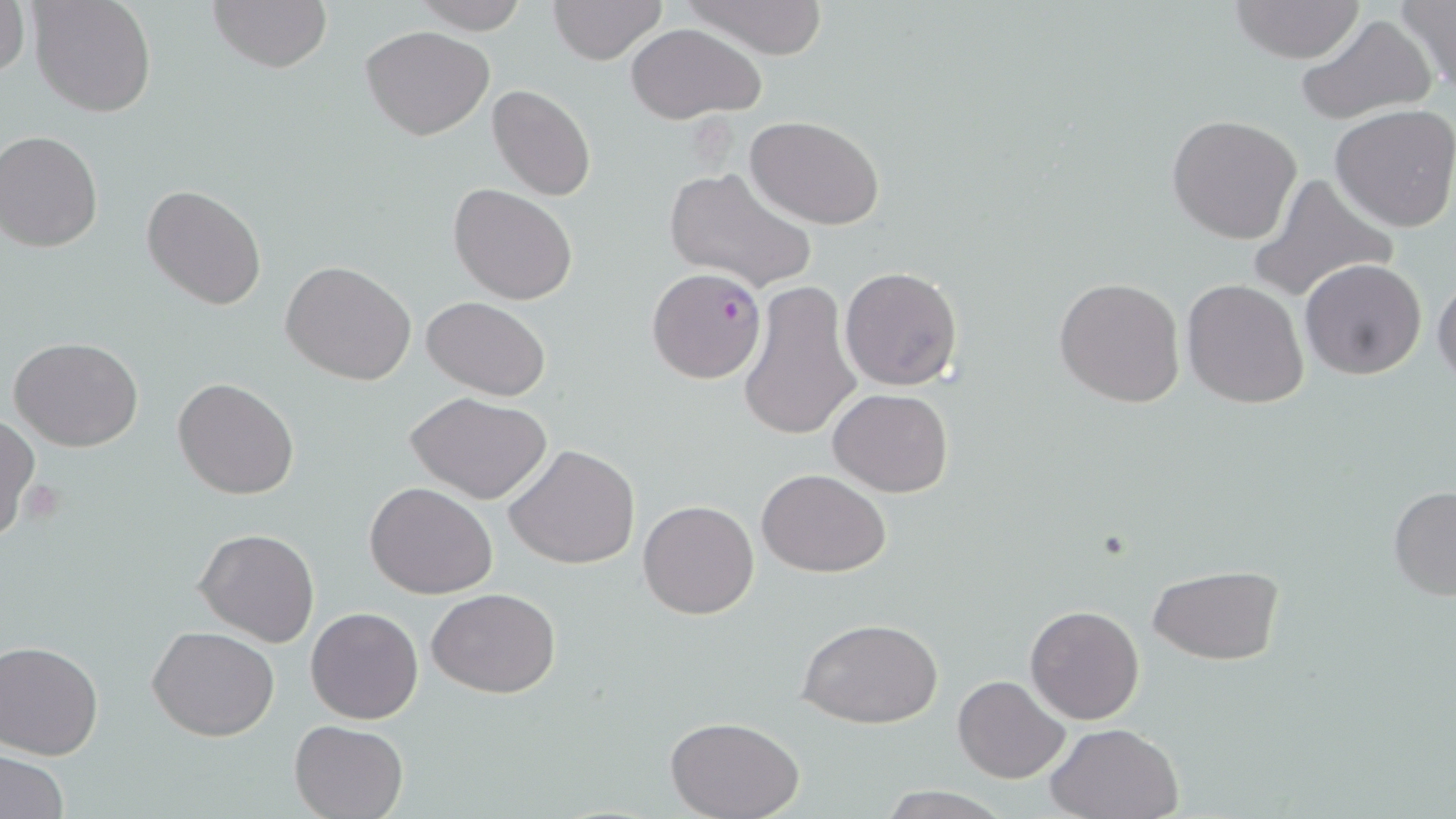
Summary:
  - Coordinate format: approximate bounding boxes as (x1,y1)-(x2,y2) corner pairs in pixels
  - Plasmodium falciparum-infected red blood cell locations: (643,267)-(763,384)
  - Platelet locations: (20,479)-(66,526)
  - Uninfected red blood cell locations: (0,0)-(28,80), (208,0)-(334,75), (547,0)-(668,65), (679,0)-(828,59), (1228,0)-(1367,65), (1395,0)-(1456,93), (27,1)-(156,117), (411,1)-(530,34), (1295,15)-(1437,126), (625,23)-(767,123), (361,26)-(494,141), (487,83)-(595,201), (1330,105)-(1456,232), (1167,114)-(1304,245), (746,116)-(885,229), (0,131)-(103,251), (663,165)-(816,293), (1246,172)-(1397,303), (141,184)-(267,311), (449,184)-(578,305), (1300,258)-(1427,380), (281,260)-(417,386), (839,266)-(963,391), (1431,270)-(1456,389), (1054,277)-(1185,407), (1182,278)-(1311,409), (737,280)-(863,443), (421,296)-(550,401), (10,336)-(144,452), (173,377)-(300,500), (829,388)-(952,497), (407,391)-(553,505), (0,414)-(39,541), (505,444)-(640,569), (758,468)-(890,577), (365,481)-(497,600), (1387,486)-(1456,601), (638,499)-(760,620), (194,528)-(321,647), (1148,566)-(1284,664), (427,586)-(561,698), (1025,605)-(1145,725), (306,607)-(424,723), (798,616)-(944,730), (148,625)-(279,742), (0,640)-(103,759), (952,675)-(1069,784), (665,716)-(805,819), (290,719)-(409,819), (1047,722)-(1185,819), (1,750)-(68,818)
  - Slide-level diagnosis: Plasmodium falciparum
  - Modality: optical microscopy
  - Magnification: 1000x
  - Field of view: one of a larger specimen
  - Image size: 1456×819 pixels
  - Stain: May-Grünwald-Giemsa
  - Preparation: thin blood smear